Identify the blood parasite species.
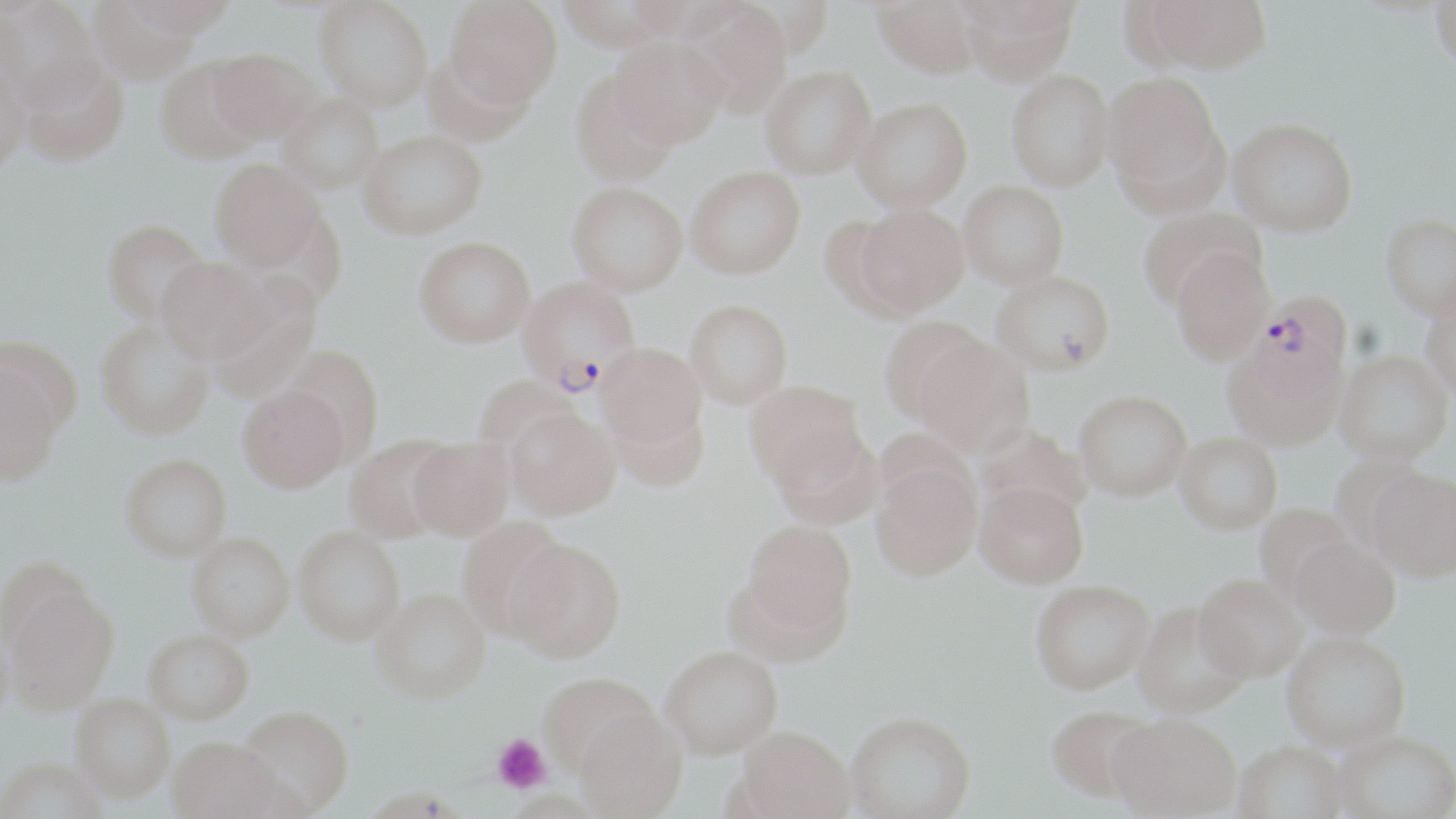
Plasmodium falciparum.

Approximate bounding boxes as (x1, y1, x2, y2) in pixels. Uninfected red blood cell locations: (122, 0, 240, 37), (314, 0, 433, 110), (871, 0, 984, 77), (957, 0, 1080, 84), (1142, 0, 1272, 73), (1, 1, 103, 111), (87, 1, 201, 83), (444, 1, 563, 108), (1431, 1, 1456, 74), (680, 2, 794, 116), (610, 37, 729, 148), (207, 48, 320, 144), (0, 49, 32, 175), (16, 55, 129, 166), (155, 57, 265, 164), (760, 66, 876, 179), (1006, 69, 1116, 190), (569, 70, 679, 186), (1102, 71, 1225, 201), (277, 93, 385, 194), (853, 97, 973, 211), (1228, 117, 1357, 236), (359, 129, 487, 238), (209, 158, 325, 273), (686, 165, 806, 278), (959, 180, 1070, 289), (567, 181, 688, 295), (855, 203, 969, 316), (1137, 206, 1265, 311), (1380, 216, 1456, 323), (101, 218, 210, 325), (414, 235, 535, 347), (1171, 249, 1274, 367), (155, 255, 277, 365), (991, 270, 1114, 376), (685, 299, 793, 407), (1421, 299, 1456, 404), (879, 318, 993, 426), (95, 320, 215, 440), (1, 336, 83, 441), (916, 339, 1035, 457), (596, 343, 707, 448), (1221, 343, 1348, 454), (281, 344, 385, 457), (1334, 355, 1454, 469), (0, 363, 64, 486), (472, 374, 579, 455), (744, 380, 867, 490), (237, 384, 350, 493), (1074, 393, 1192, 503), (609, 400, 711, 492), (505, 408, 620, 519), (976, 423, 1091, 523), (771, 429, 883, 530), (343, 434, 456, 543), (1174, 436, 1282, 538), (407, 437, 515, 539), (120, 453, 232, 561), (871, 460, 982, 584), (1367, 474, 1456, 586), (973, 485, 1089, 593), (1254, 506, 1356, 604), (456, 516, 569, 638), (741, 519, 857, 639), (294, 525, 405, 644), (187, 532, 295, 641), (502, 536, 626, 661), (1289, 540, 1400, 644), (1194, 579, 1305, 686), (4, 584, 120, 713), (1030, 584, 1154, 699), (372, 587, 491, 704), (1132, 606, 1251, 722), (143, 629, 254, 724), (1282, 636, 1411, 756), (660, 644, 783, 758), (539, 672, 659, 777), (70, 695, 175, 803), (237, 705, 355, 815), (574, 708, 687, 818), (1045, 709, 1156, 808), (846, 717, 976, 819), (1107, 719, 1240, 819), (735, 728, 854, 819), (1331, 736, 1456, 819), (168, 737, 288, 819), (1232, 746, 1349, 819), (0, 760, 108, 819). Plasmodium falciparum-infected red blood cell locations: (517, 276, 641, 393), (1248, 293, 1353, 398). Platelet locations: (492, 734, 551, 794). One field of a larger specimen. Image is 1456×819 pixels. May-Grünwald-Giemsa stain. Light microscopy. Thin blood smear. Captured at 1000x magnification.